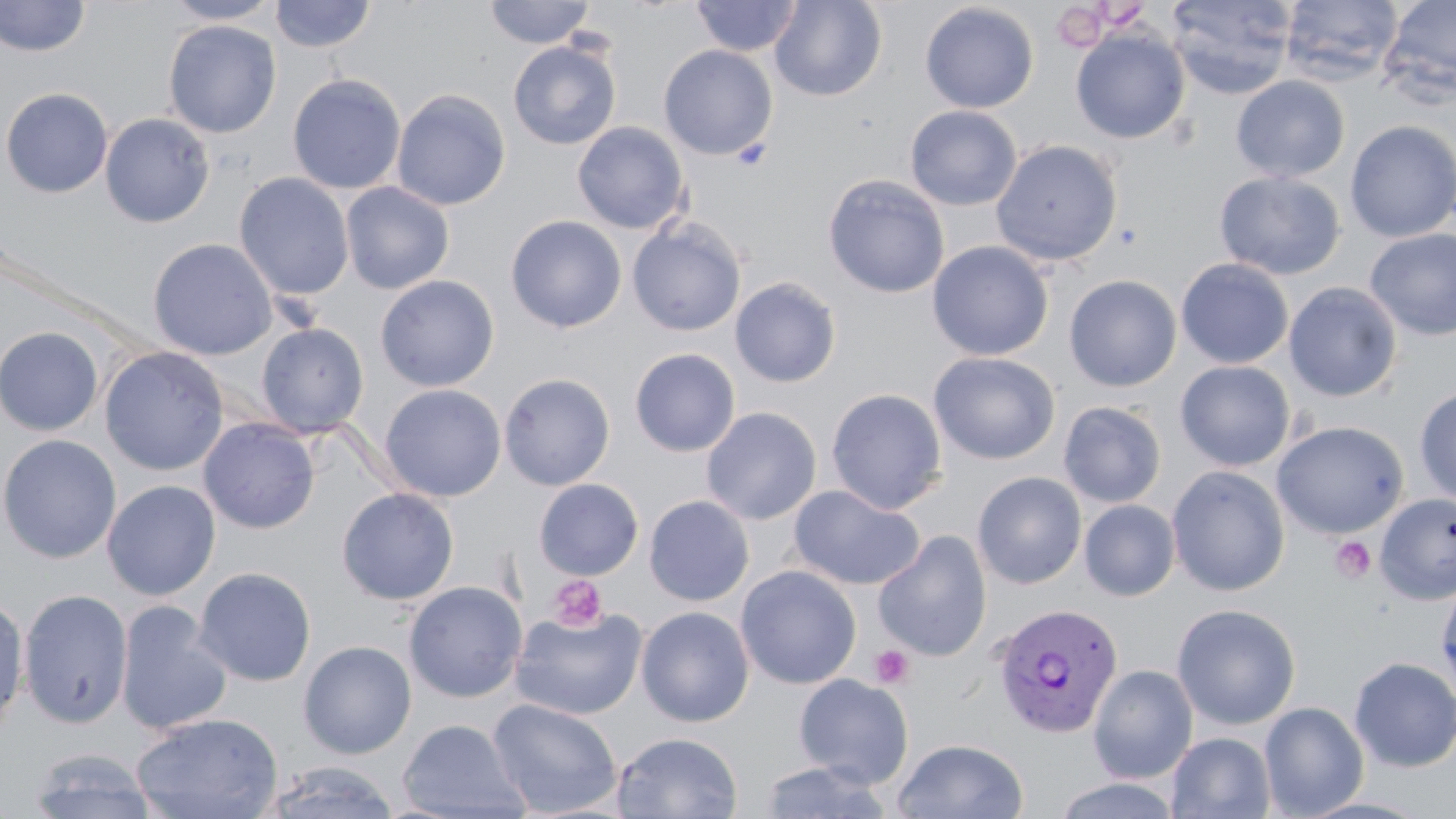
Approximate bounding boxes as [x1, y1, x2, y2] in pixels. Plasmodium vivax-infected red blood cell locations: [991, 602, 1124, 738]. Platelet locations: [1052, 4, 1108, 51], [1330, 535, 1376, 583], [547, 575, 606, 631], [869, 645, 914, 689]. Uninfected red blood cell locations: [1, 0, 91, 57], [163, 0, 282, 24], [270, 0, 376, 53], [484, 0, 596, 48], [690, 0, 804, 57], [769, 0, 887, 102], [1166, 0, 1297, 99], [1280, 0, 1403, 83], [1380, 0, 1456, 101], [920, 3, 1039, 113], [163, 20, 282, 138], [1070, 28, 1190, 144], [507, 40, 621, 150], [658, 44, 778, 159], [287, 74, 406, 195], [1231, 75, 1350, 183], [0, 87, 113, 198], [391, 89, 510, 210], [904, 105, 1022, 211], [100, 113, 215, 228], [1344, 120, 1456, 243], [572, 122, 690, 234], [990, 139, 1123, 267], [1214, 171, 1346, 280], [234, 173, 355, 301], [823, 174, 950, 299], [340, 182, 454, 294], [505, 215, 627, 333], [627, 218, 746, 337], [1364, 228, 1456, 340], [148, 238, 278, 360], [927, 241, 1054, 361], [1176, 258, 1294, 369], [375, 274, 499, 392], [1064, 275, 1182, 392], [729, 277, 842, 388], [1283, 281, 1403, 402], [256, 323, 369, 438], [0, 326, 104, 436], [99, 346, 229, 476], [630, 348, 740, 457], [928, 351, 1061, 465], [1175, 361, 1296, 471], [499, 372, 615, 490], [379, 384, 506, 501], [1413, 385, 1456, 505], [826, 388, 947, 513], [1058, 401, 1167, 507], [701, 406, 822, 525], [198, 418, 320, 534], [1271, 420, 1409, 539], [0, 434, 121, 564], [1167, 465, 1290, 597], [972, 471, 1087, 589], [533, 479, 644, 580], [101, 480, 221, 600], [789, 485, 925, 590], [337, 487, 458, 605], [1374, 493, 1456, 605], [644, 495, 754, 606], [1079, 499, 1181, 601], [873, 531, 992, 662], [736, 565, 861, 689], [194, 568, 316, 686], [1437, 577, 1456, 700], [403, 582, 527, 702], [18, 588, 134, 729], [0, 594, 30, 734], [115, 600, 232, 735], [1172, 603, 1301, 729], [510, 604, 648, 720], [636, 606, 755, 727], [298, 640, 417, 760], [1349, 657, 1456, 772], [1087, 664, 1198, 783], [793, 673, 914, 788], [487, 697, 623, 818], [1259, 701, 1369, 818], [132, 713, 283, 819], [397, 719, 529, 819], [612, 731, 742, 819], [1167, 731, 1276, 819], [891, 738, 1029, 818], [27, 747, 157, 819], [757, 760, 894, 818], [261, 761, 400, 819], [1051, 776, 1185, 818]. Slide-level diagnosis: Plasmodium vivax. Optical microscopy. May-Grünwald-Giemsa stain. Image is 1456×819 pixels. Captured at 1000x magnification. Thin blood film. One field of a larger specimen.